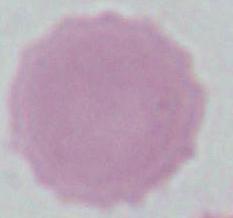

A red blood cell is seen. Captured at 1000x magnification. Photomicrograph.